Report the malaria status of this cell.
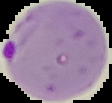

It is parasitized.

preparation = thin blood film
image size = 112×103 pixels
image type = segmented cell region on a black background